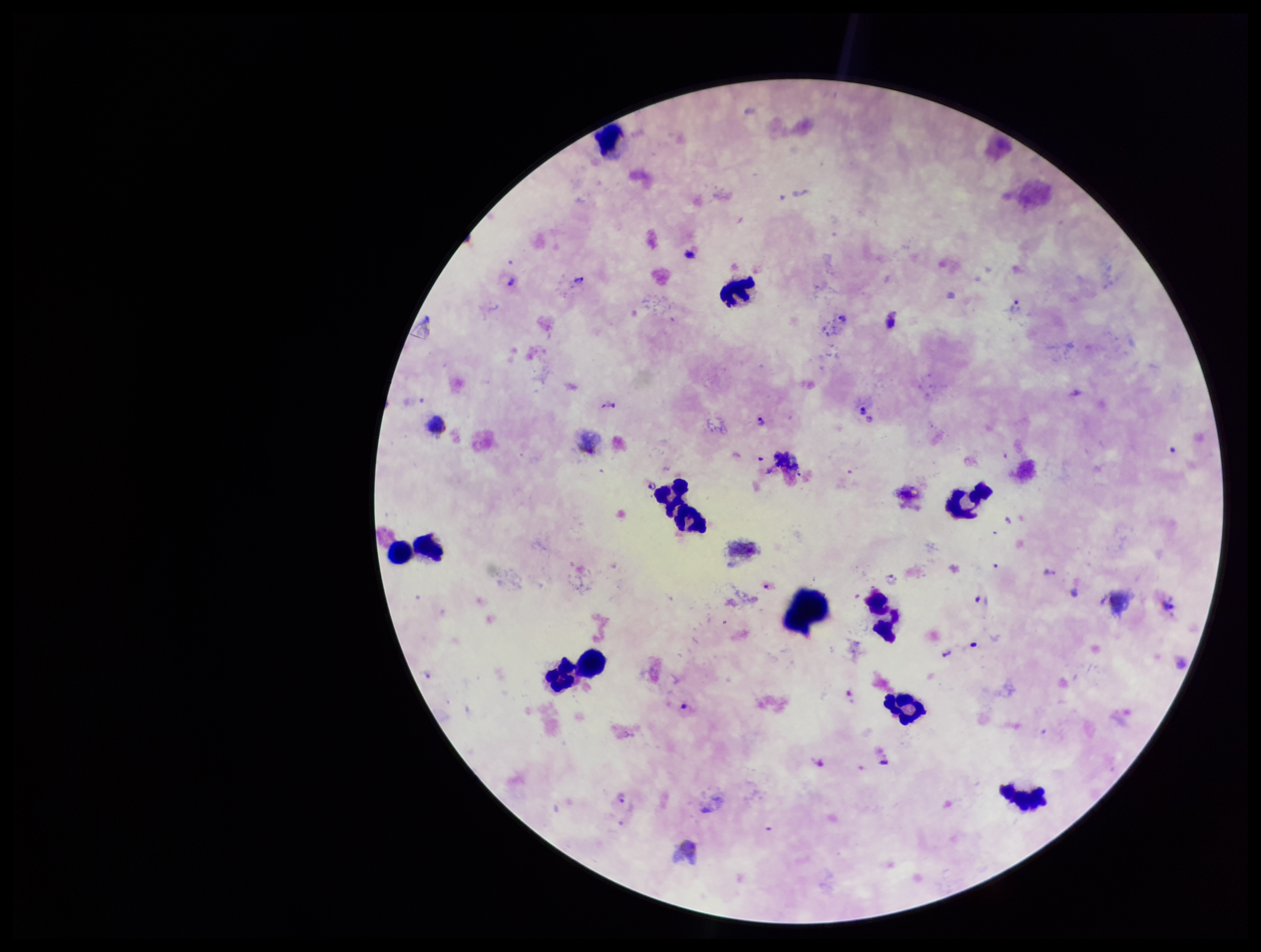

parasite_count: 10
field_of_view: single
stain: Giemsa
patient_malaria_status: positive
image_size: 1261×952 pixels
plasmodium_parasites: detected
capture: smartphone photograph through the microscope eyepiece
species_reported_for_this_patient: Plasmodium vivax
preparation: thick smear
leukocyte_count: 11